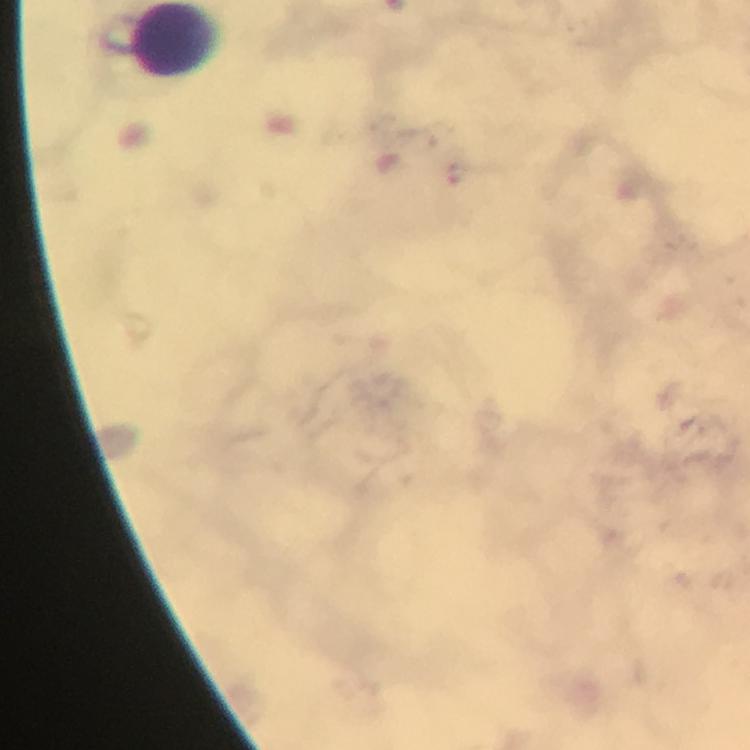

{
  "leukocyte_locations": "approximate centers as [x, y] in pixels: [175, 39]",
  "preparation": "thick blood smear",
  "context": "from a diagnostic examination for malaria",
  "image_size": "750×750 pixels",
  "plasmodium_parasites": "none seen",
  "stain": "Giemsa",
  "capture": "smartphone photograph through a microscope",
  "magnification": "100x",
  "immersion_oil": "applied",
  "cropped_from": "one field of view"
}